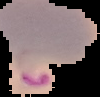
{
  "image_type": "segmented cell region on a black background",
  "preparation": "thin blood smear",
  "image_size": "100×97 pixels",
  "malaria_status": "parasitized"
}